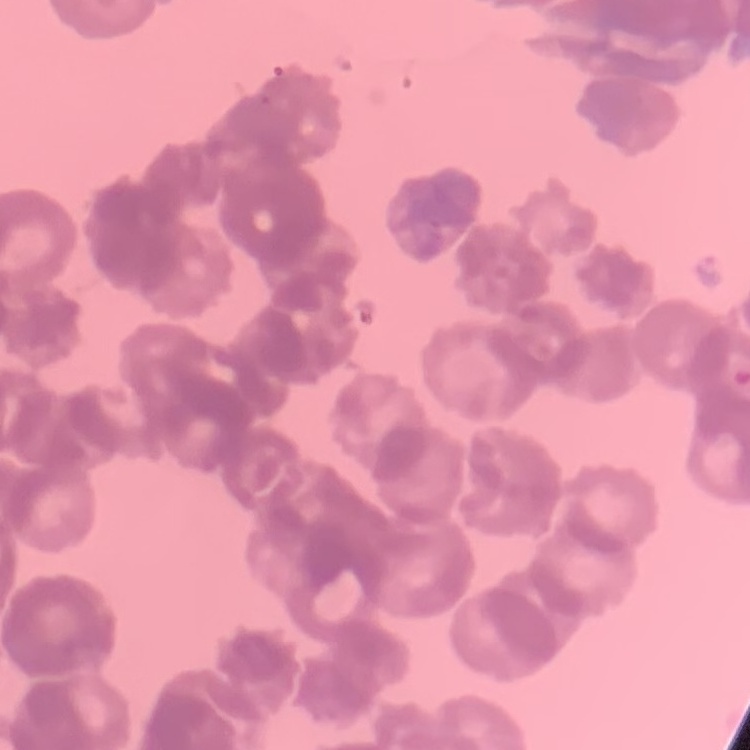

{
  "red_blood_cell_morphology": "rouleaux formation",
  "stain": "Field's or Giemsa",
  "preparation": "thin blood smear",
  "image_type": "one tile cut from a larger photomicrograph"
}